Assess this cell for malaria.
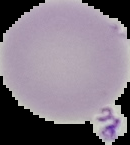
Uninfected.

image size = 130×145 pixels
preparation = thin blood smear
image type = cell region segmented out of the field of view; surrounding area masked to black